Report the malaria status of this cell.
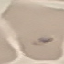

Parasitized.

Summary:
  - Stain: Giemsa
  - Image type: automatically extracted cell patch, resized to 64 × 64 pixels
  - Preparation: thin smear
  - Capture: smartphone camera at the microscope eyepiece